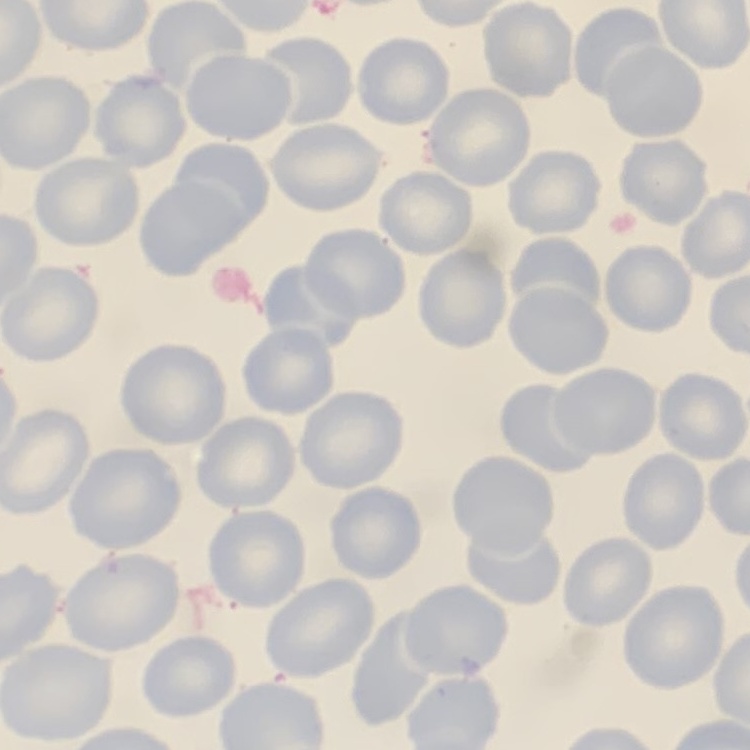
Summary:
  - Erythrocyte morphology: no rouleaux formation
  - Preparation: thin blood film
  - Image type: square crop of a larger photomicrograph
  - Stain: Field's or Giemsa